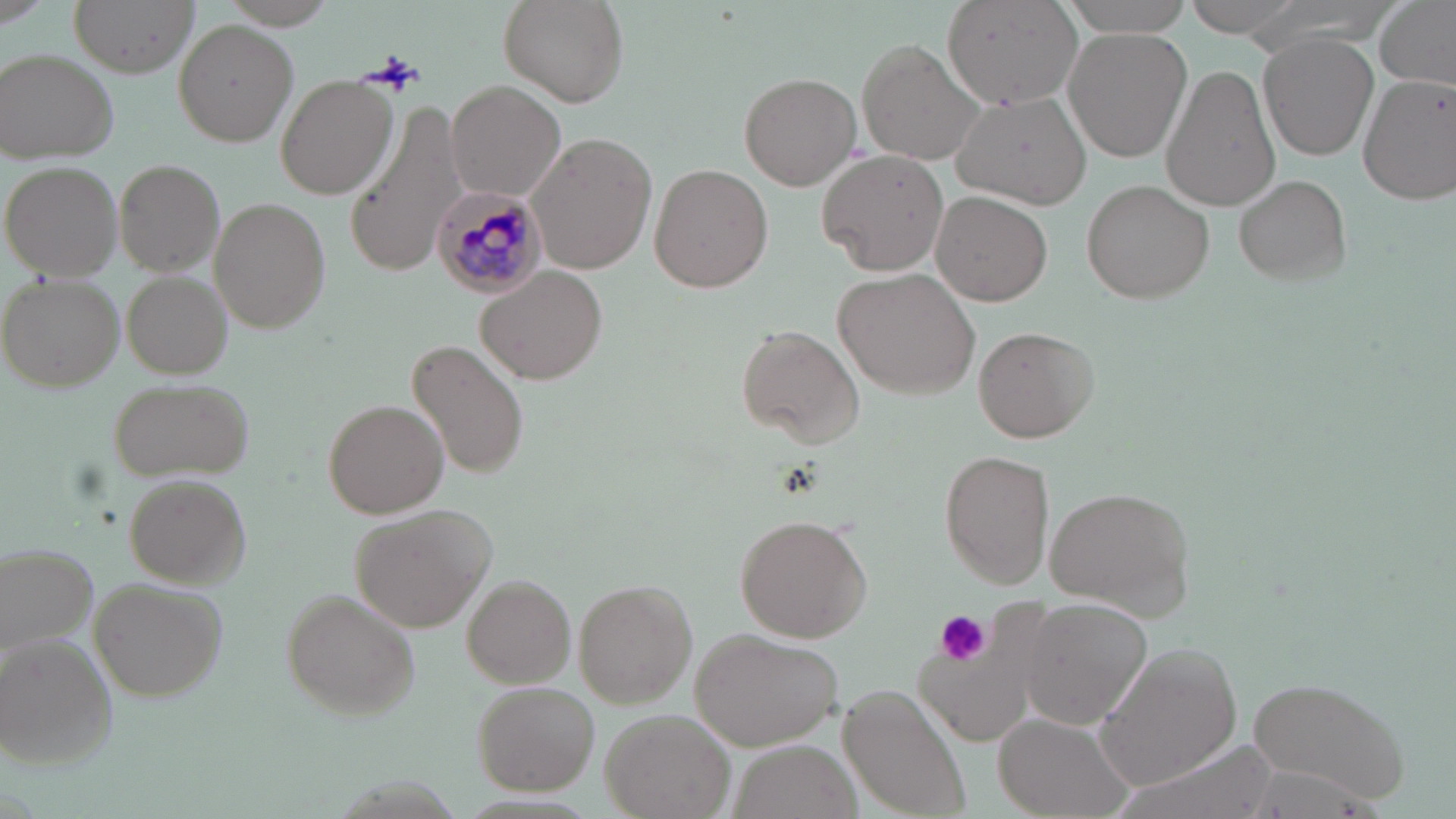
Summary:
  - Coordinate format: approximate bounding boxes as named x1/y1/x2/y2 corners in pixels
  - Uninfected red blood cell locations: (x1=71, y1=0, x2=198, y2=75), (x1=496, y1=0, x2=629, y2=109), (x1=1056, y1=0, x2=1197, y2=34), (x1=1184, y1=0, x2=1308, y2=35), (x1=1373, y1=0, x2=1455, y2=91), (x1=945, y1=1, x2=1084, y2=110), (x1=176, y1=19, x2=298, y2=147), (x1=1063, y1=28, x2=1192, y2=161), (x1=1261, y1=33, x2=1378, y2=161), (x1=861, y1=40, x2=986, y2=166), (x1=1, y1=50, x2=120, y2=163), (x1=1161, y1=63, x2=1281, y2=214), (x1=738, y1=71, x2=860, y2=189), (x1=276, y1=74, x2=398, y2=201), (x1=1359, y1=74, x2=1456, y2=205), (x1=445, y1=81, x2=566, y2=202), (x1=952, y1=91, x2=1092, y2=208), (x1=349, y1=96, x2=472, y2=273), (x1=528, y1=134, x2=657, y2=272), (x1=818, y1=149, x2=952, y2=277), (x1=3, y1=160, x2=121, y2=279), (x1=115, y1=161, x2=224, y2=277), (x1=650, y1=163, x2=773, y2=293), (x1=1236, y1=174, x2=1352, y2=288), (x1=1081, y1=179, x2=1214, y2=305), (x1=932, y1=191, x2=1054, y2=308), (x1=211, y1=198, x2=330, y2=333), (x1=477, y1=265, x2=605, y2=384), (x1=833, y1=270, x2=980, y2=398), (x1=122, y1=272, x2=232, y2=379), (x1=2, y1=277, x2=125, y2=392), (x1=737, y1=324, x2=866, y2=450), (x1=975, y1=327, x2=1098, y2=441), (x1=409, y1=339, x2=528, y2=478), (x1=105, y1=377, x2=258, y2=484), (x1=325, y1=400, x2=447, y2=518), (x1=939, y1=451, x2=1054, y2=588), (x1=125, y1=474, x2=252, y2=586), (x1=1045, y1=486, x2=1197, y2=616), (x1=354, y1=504, x2=496, y2=631), (x1=735, y1=514, x2=874, y2=643), (x1=1, y1=543, x2=98, y2=654), (x1=462, y1=575, x2=574, y2=689), (x1=91, y1=578, x2=227, y2=700), (x1=572, y1=581, x2=695, y2=707), (x1=282, y1=592, x2=422, y2=719), (x1=1019, y1=598, x2=1153, y2=730), (x1=694, y1=631, x2=841, y2=750), (x1=0, y1=635, x2=118, y2=770), (x1=1096, y1=641, x2=1244, y2=792), (x1=1241, y1=674, x2=1412, y2=806), (x1=473, y1=681, x2=601, y2=795), (x1=837, y1=686, x2=968, y2=818), (x1=600, y1=709, x2=738, y2=819), (x1=994, y1=713, x2=1137, y2=819)
  - Platelet locations: (x1=369, y1=53, x2=425, y2=92), (x1=935, y1=610, x2=993, y2=667)
  - Plasmodium malariae-infected red blood cell locations: (x1=430, y1=185, x2=549, y2=298)
  - Slide-level diagnosis: Plasmodium malariae
  - Stain: May-Grünwald-Giemsa
  - Image size: 1456×819 pixels
  - Magnification: 1000x
  - Modality: light microscopy
  - Field of view: one of a larger specimen
  - Preparation: thin blood smear